Locate every Plasmodium falciparum-infected red blood cell.
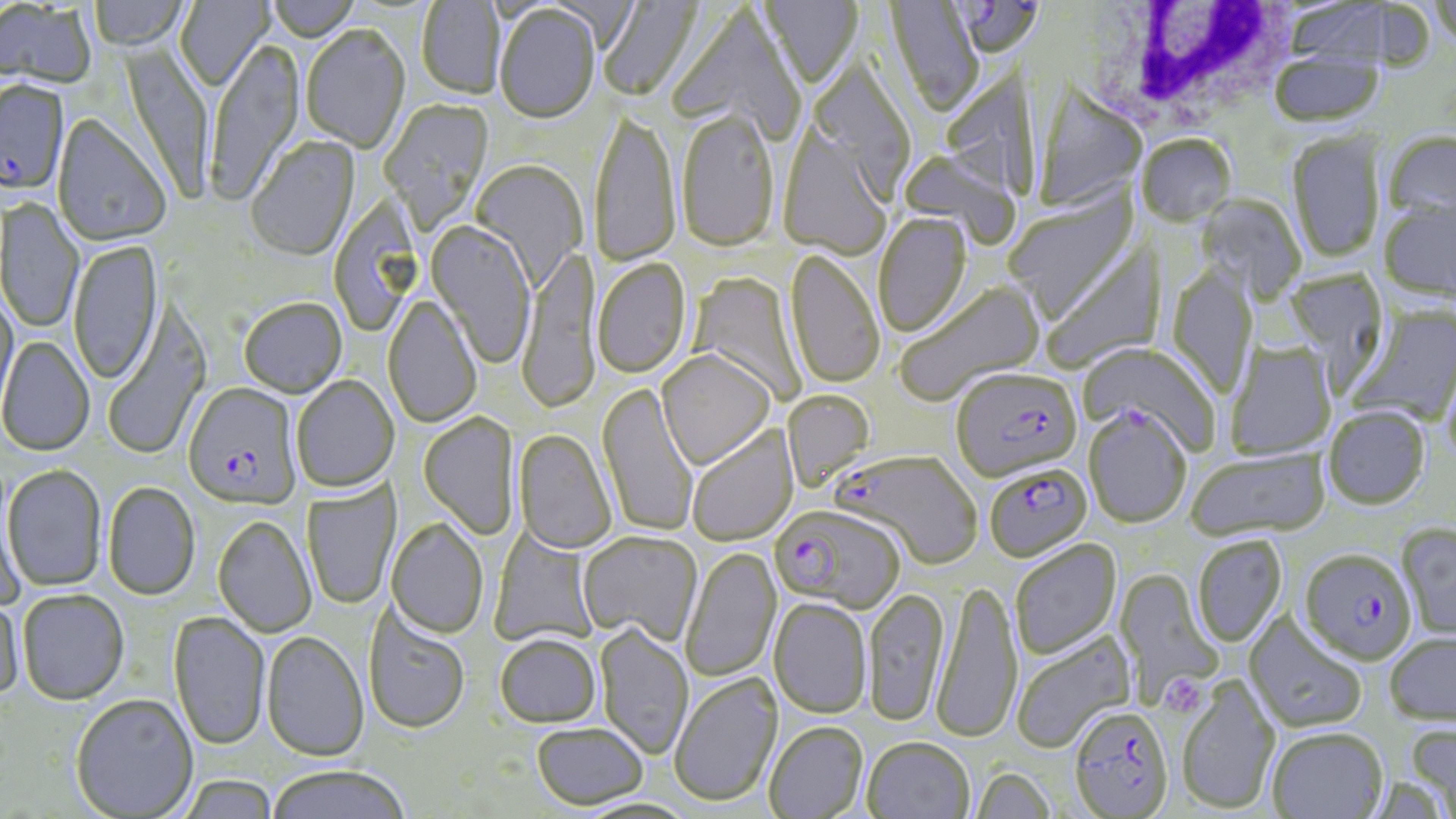

Approximate bounding boxes as [x1, y1, x2, y2] in pixels.
Plasmodium falciparum-infected red blood cells: [954, 0, 1045, 71], [1, 81, 69, 199], [950, 367, 1082, 483], [183, 384, 301, 510], [1084, 407, 1191, 528], [836, 450, 983, 571], [988, 466, 1096, 564], [771, 505, 904, 614], [1300, 548, 1417, 664], [1074, 707, 1179, 819].

{
  "slide_level_diagnosis": "Plasmodium falciparum",
  "field_of_view": "one of a larger specimen",
  "platelet_locations": "approximate bounding boxes as [x1, y1, x2, y2] in pixels: [1164, 676, 1202, 715]",
  "modality": "light microscopy",
  "white_blood_cell_locations": "approximate bounding boxes as [x1, y1, x2, y2] in pixels: [1072, 4, 1299, 138]",
  "uninfected_red_blood_cell_locations": "approximate bounding boxes as [x1, y1, x2, y2] in pixels: [90, 0, 190, 53], [174, 0, 274, 93], [266, 0, 359, 44], [598, 0, 705, 102], [759, 0, 863, 91], [1429, 0, 1456, 50], [416, 1, 504, 100], [885, 1, 983, 119], [1284, 1, 1401, 66], [0, 2, 96, 91], [495, 6, 600, 126], [666, 7, 804, 141], [301, 27, 410, 155], [207, 42, 305, 206], [120, 43, 213, 203], [1269, 51, 1385, 128], [944, 52, 1037, 203], [810, 60, 916, 203], [1032, 80, 1146, 211], [378, 98, 494, 233], [678, 113, 778, 254], [589, 114, 682, 269], [53, 115, 170, 247], [779, 126, 892, 261], [1383, 130, 1456, 224], [1287, 131, 1386, 263], [1137, 135, 1237, 227], [246, 136, 360, 262], [898, 149, 1022, 248], [470, 161, 587, 290], [1003, 186, 1140, 323], [1197, 193, 1306, 304], [1, 199, 84, 334], [1378, 199, 1456, 302], [875, 213, 972, 339], [426, 222, 536, 369], [69, 240, 164, 386], [1041, 241, 1167, 374], [516, 247, 601, 416], [785, 249, 884, 391], [592, 258, 692, 380], [1167, 264, 1258, 401], [1283, 269, 1390, 392], [688, 272, 807, 405], [894, 280, 1045, 406], [0, 287, 18, 418], [382, 296, 482, 428], [239, 299, 347, 398], [102, 303, 211, 462], [1346, 305, 1456, 427], [0, 336, 95, 456], [1080, 342, 1220, 454], [1225, 342, 1337, 460], [657, 351, 775, 469], [291, 375, 399, 493], [597, 382, 699, 538], [782, 390, 875, 491], [1323, 406, 1430, 509], [418, 413, 520, 541], [686, 425, 798, 547], [514, 429, 617, 554], [1187, 448, 1329, 542], [3, 464, 107, 592], [1, 475, 26, 609], [301, 478, 401, 610], [103, 482, 201, 601], [212, 515, 317, 638], [387, 517, 489, 639], [1397, 522, 1456, 640], [490, 528, 600, 648], [577, 531, 702, 646], [1193, 535, 1288, 648], [1009, 539, 1121, 661], [680, 546, 782, 683], [1114, 569, 1225, 708], [931, 581, 1022, 746], [863, 588, 949, 727], [16, 589, 129, 705], [0, 594, 25, 703], [769, 599, 872, 719], [364, 606, 470, 734], [168, 611, 270, 751], [1244, 613, 1367, 734], [595, 623, 693, 760], [1010, 630, 1137, 755], [261, 631, 369, 761], [1384, 632, 1456, 725], [494, 633, 602, 727], [669, 672, 783, 807], [1176, 676, 1282, 814], [70, 694, 198, 818], [764, 721, 868, 819], [532, 722, 648, 810], [1406, 723, 1456, 815], [1267, 727, 1388, 819], [862, 738, 974, 819], [266, 764, 410, 819], [970, 768, 1055, 819], [179, 774, 278, 819], [575, 796, 699, 818]",
  "image_size": "1456×819 pixels",
  "preparation": "thin blood film",
  "stain": "May-Grünwald-Giemsa",
  "magnification": "1000x"
}